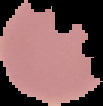

From a thin blood smear. Result: no Plasmodium parasites seen. Image is 103×106 pixels. The area outside the segmented cell region is set to black.